Name the parasite shown.
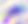

This is Toxoplasma gondii.

magnification: 400x
modality: photomicrograph